State which cell type is depicted.
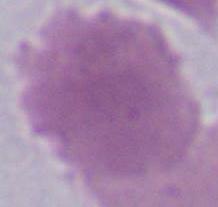
This is an erythrocyte.

Summary:
  - Modality: photomicrograph
  - Magnification: 1000x